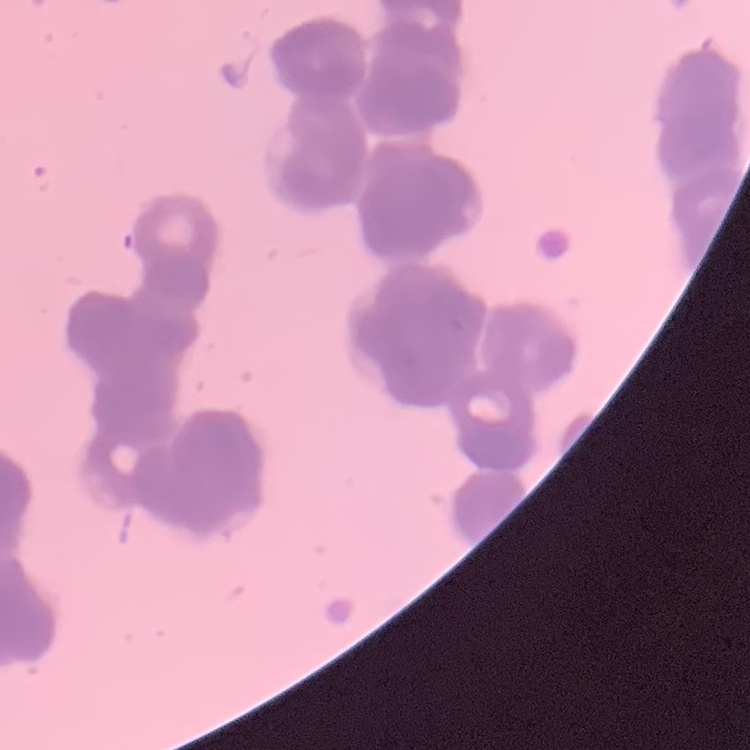 The red blood cells show rouleaux formation. One tile cut from a larger photomicrograph. Field's or Giemsa stain. Thin blood film.